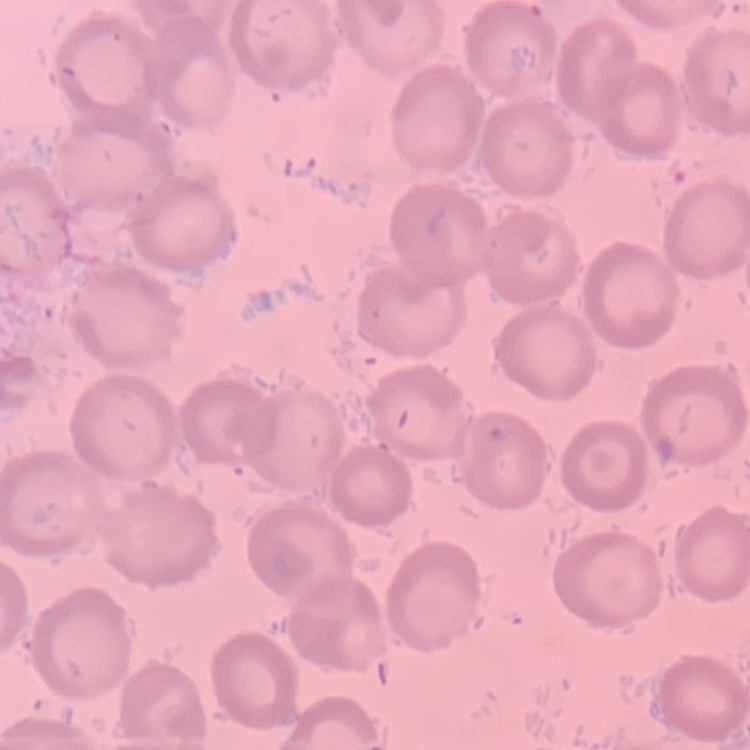
erythrocyte_morphology: no rouleaux formation
image_type: one tile cut from a larger photomicrograph
preparation: thin blood smear
stain: Field's or Giemsa